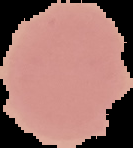
{
  "result": "no Plasmodium parasites detected",
  "preparation": "thin blood smear",
  "image_type": "segmented cell region on a black background",
  "image_size": "133×148 pixels"
}